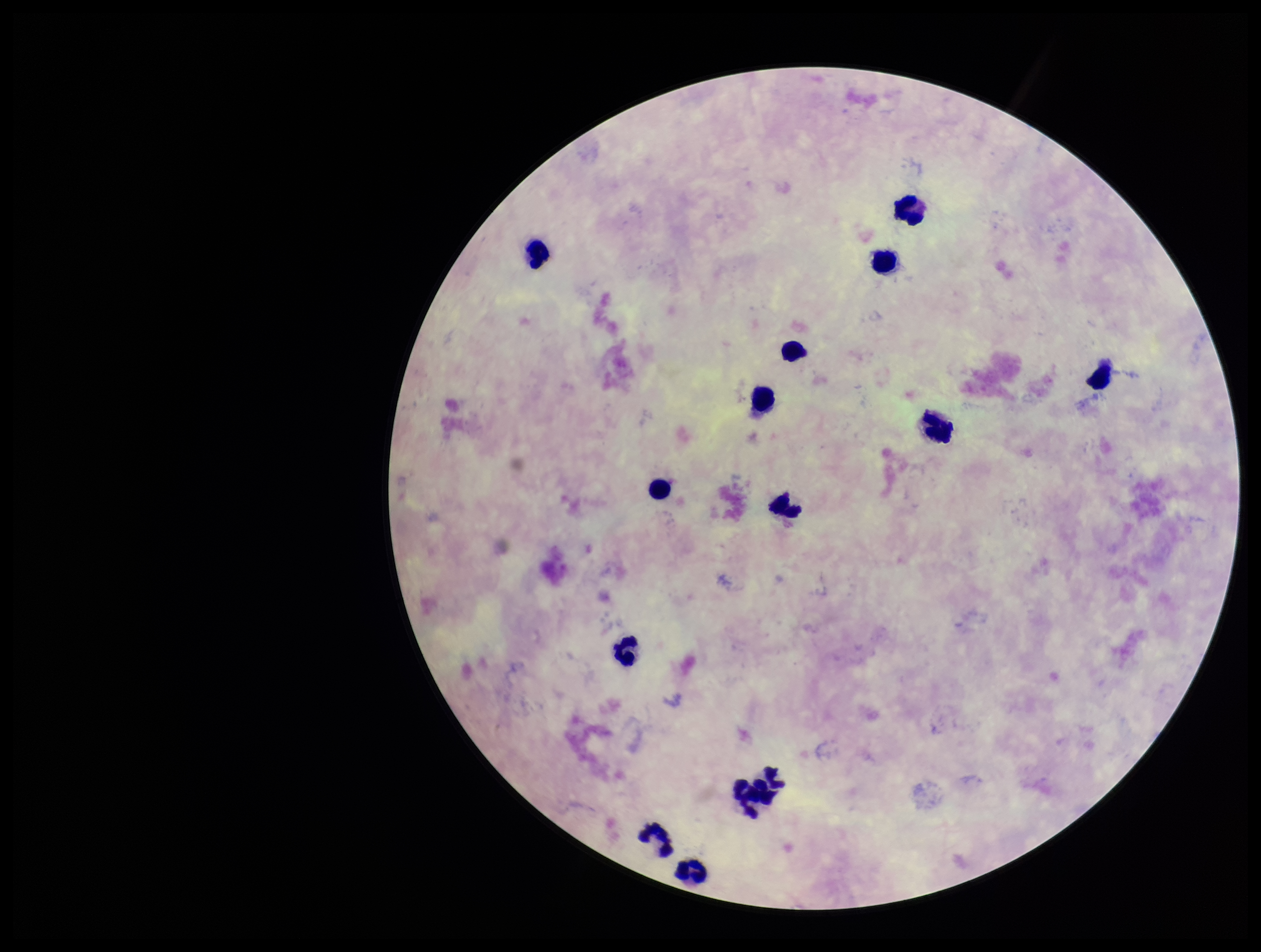

Summary:
  - Plasmodium parasites: none detected
  - Stain: Giemsa
  - Parasite count: 0
  - Capture: smartphone photograph through the microscope eyepiece
  - Patient malaria status: negative
  - Leukocyte count: 14
  - Preparation: thick smear
  - Field of view: one from this slide
  - Image size: 1261×952 pixels